Assess this cell for malaria.
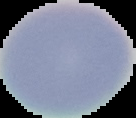
Uninfected.

Image is 136×118 pixels. From a thin blood film. Cell region segmented out of the field of view; the surrounding area is masked to black.